Identify the blood parasite species.
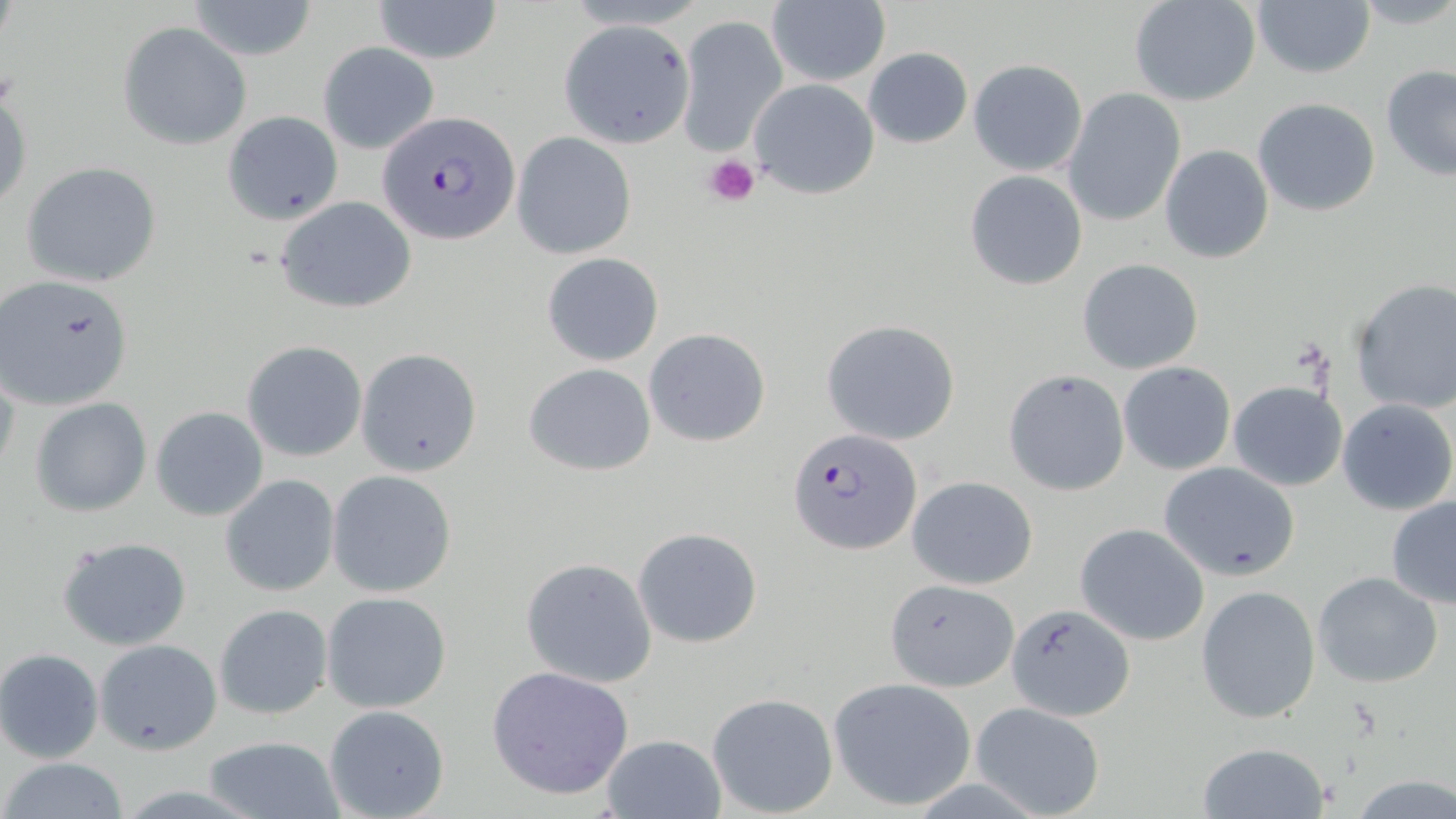

Plasmodium falciparum.

Approximate bounding boxes as (x1,y1)-(x2,y2) corner pairs in pixels. Plasmodium falciparum-infected red blood cell locations: (378,110)-(520,245), (789,429)-(923,554). Uninfected red blood cell locations: (186,0)-(319,61), (372,0)-(504,64), (767,0)-(891,86), (1128,0)-(1262,107), (1251,0)-(1375,79), (1349,0)-(1456,32), (674,15)-(786,154), (557,18)-(695,149), (117,21)-(251,150), (317,42)-(440,155), (862,48)-(973,148), (968,59)-(1088,176), (1381,65)-(1456,181), (748,78)-(880,200), (0,83)-(31,215), (1062,87)-(1185,227), (1252,98)-(1382,217), (222,110)-(343,226), (513,131)-(636,259), (1160,144)-(1274,264), (21,161)-(162,288), (964,169)-(1087,289), (277,197)-(418,313), (541,252)-(664,367), (1077,259)-(1203,373), (1,275)-(134,412), (1349,278)-(1456,415), (822,318)-(962,446), (644,327)-(771,447), (241,340)-(367,462), (357,347)-(482,475), (1119,361)-(1235,474), (523,362)-(657,477), (0,364)-(21,489), (1003,369)-(1129,496), (1228,380)-(1347,490), (30,397)-(153,517), (1337,399)-(1455,516), (151,406)-(270,522), (1158,461)-(1301,582), (327,471)-(457,596), (220,475)-(341,595), (906,475)-(1038,589), (1386,495)-(1456,607), (1075,523)-(1209,646), (633,527)-(763,648), (57,535)-(193,650), (521,557)-(658,688), (1312,571)-(1444,690), (883,579)-(1020,692), (1196,585)-(1323,725), (321,591)-(453,713), (1008,602)-(1135,720), (213,603)-(333,719), (93,638)-(223,754), (0,648)-(104,762), (486,665)-(634,798), (827,677)-(976,812), (706,692)-(839,815), (970,701)-(1106,818), (322,705)-(450,819), (599,733)-(726,819), (206,734)-(343,817), (1196,740)-(1331,818), (0,757)-(132,818), (1347,775)-(1456,817). Platelet locations: (703,153)-(760,209). May-Grünwald-Giemsa-stained preparation. Image is 1456×819 pixels. Light microscopy. Thin blood smear. One field of a larger specimen. Captured at 1000x magnification.